Locate every Plasmodium falciparum parasite and give its life-cycle stage, and locate every leukocyte and any debris.
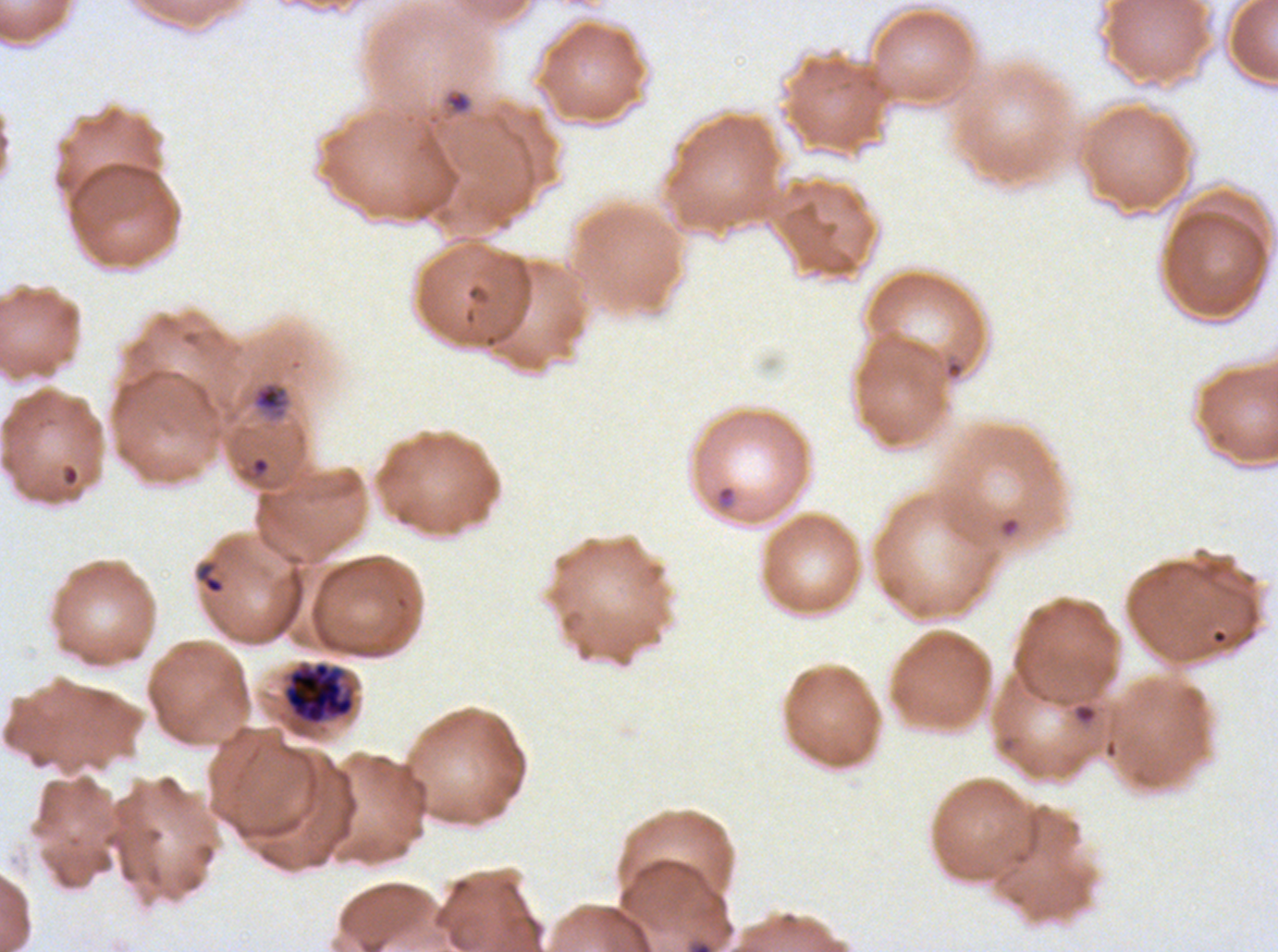
Approximate bounding boxes as (x1, y1, x2, y2) in pixels.
Rings: (196, 561, 225, 594).
Late-ring/early-trophozoite forms: (445, 91, 472, 114), (252, 381, 290, 420).
Late schizonts: (285, 662, 354, 724).
No mid trophozoites, late trophozoites, early schizonts, segmenters, gametocytes, leukocytes, or debris observed.

{
  "stain": "Giemsa",
  "preparation": "thin blood smear",
  "image_size": "1278×952 pixels",
  "life_cycle_stages_observed": "ring, late-ring/early-trophozoite, late schizont",
  "specimen": "Plasmodium falciparum from a patient in The Gambia, cultured ex vivo for 24 to 48 hours",
  "field_of_view": "sub-image separated from a larger composite"
}